Identify the blood parasite species.
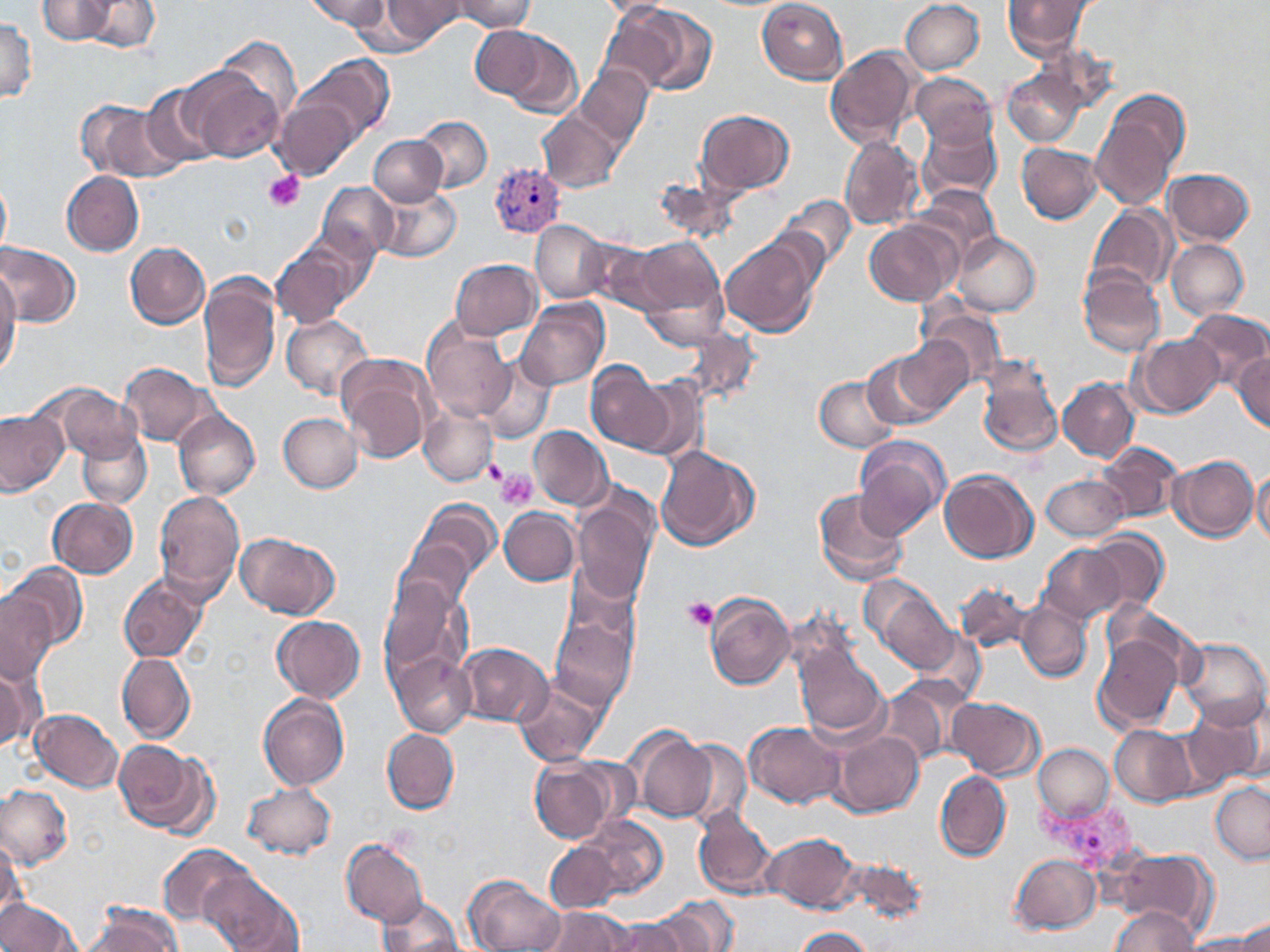

Plasmodium vivax.

field of view = single
Plasmodium vivax-infected red blood cell locations = approximate bounding boxes as [x1, y1, x2, y2] in pixels: [489, 162, 565, 238], [1030, 797, 1146, 877]
platelet locations = approximate bounding boxes as [x1, y1, x2, y2] in pixels: [263, 172, 305, 213], [483, 457, 508, 485], [497, 470, 538, 510], [682, 596, 719, 631]
magnification = 1000x
image size = 1270×952 pixels
uninfected red blood cell locations = approximate bounding boxes as [x1, y1, x2, y2] in pixels: [36, 0, 119, 44], [80, 0, 159, 54], [308, 0, 391, 29], [377, 0, 468, 47], [452, 0, 535, 32], [901, 0, 985, 75], [1000, 0, 1097, 61], [757, 1, 848, 83], [608, 3, 714, 100], [2, 14, 37, 103], [471, 26, 545, 98], [496, 31, 582, 119], [826, 47, 919, 149], [296, 56, 390, 145], [575, 65, 651, 149], [183, 66, 285, 164], [1003, 66, 1089, 149], [910, 73, 998, 151], [139, 84, 223, 171], [1091, 87, 1192, 214], [276, 97, 361, 180], [74, 99, 174, 181], [696, 109, 794, 195], [537, 112, 619, 192], [414, 117, 492, 193], [916, 118, 1004, 206], [369, 134, 447, 206], [838, 135, 924, 231], [1016, 142, 1101, 223], [1164, 167, 1255, 246], [61, 171, 144, 256], [0, 177, 11, 256], [317, 182, 398, 261], [913, 184, 1003, 267], [375, 186, 461, 264], [774, 192, 856, 280], [1086, 208, 1175, 295], [531, 219, 607, 302], [865, 220, 960, 306], [953, 231, 1040, 317], [720, 235, 820, 339], [630, 237, 726, 340], [1166, 239, 1250, 320], [125, 242, 210, 327], [0, 243, 82, 327], [272, 246, 355, 328], [452, 259, 541, 339], [1078, 268, 1164, 358], [0, 271, 21, 375], [199, 273, 280, 392], [517, 299, 609, 390], [920, 304, 1009, 389], [1183, 309, 1269, 391], [281, 313, 374, 400], [422, 319, 516, 423], [679, 322, 761, 406], [894, 333, 973, 415], [1130, 334, 1222, 418], [366, 336, 513, 449], [861, 347, 955, 433], [1232, 350, 1270, 433], [336, 352, 438, 463], [477, 356, 556, 443], [977, 357, 1065, 460], [120, 362, 210, 446], [587, 363, 675, 452], [815, 376, 901, 451], [1058, 378, 1138, 461], [40, 384, 141, 460], [421, 405, 497, 485], [173, 408, 260, 500], [0, 409, 69, 497], [279, 413, 364, 492], [529, 425, 611, 511], [77, 431, 150, 507], [852, 436, 948, 538], [1099, 442, 1182, 523], [655, 444, 761, 552], [1168, 454, 1259, 542], [939, 469, 1038, 563], [1249, 469, 1269, 548], [1041, 472, 1129, 542], [812, 487, 911, 587], [153, 489, 247, 602], [571, 491, 657, 609], [48, 497, 138, 578], [397, 497, 503, 616], [498, 507, 580, 585], [1086, 530, 1168, 613], [236, 533, 340, 621], [1038, 543, 1130, 626], [3, 562, 87, 654], [118, 573, 207, 663], [863, 576, 961, 675], [379, 577, 472, 697], [955, 583, 1038, 657], [705, 592, 796, 690], [0, 594, 55, 687], [1016, 600, 1092, 684], [549, 609, 639, 713], [272, 617, 366, 703], [1093, 633, 1183, 729], [1180, 637, 1269, 729], [458, 641, 552, 727], [795, 648, 891, 744], [389, 651, 477, 736], [116, 652, 195, 743], [0, 657, 42, 749], [877, 676, 972, 768], [514, 680, 607, 765], [257, 691, 350, 792], [948, 696, 1043, 780], [1182, 704, 1265, 790], [30, 709, 123, 791], [743, 721, 845, 809], [1110, 726, 1198, 809], [382, 729, 460, 812], [835, 729, 923, 816], [633, 730, 717, 824], [681, 739, 749, 827], [111, 740, 216, 838], [1032, 743, 1115, 823], [528, 756, 619, 843], [935, 770, 1011, 861], [1209, 779, 1270, 863], [243, 783, 337, 861], [0, 784, 71, 871], [694, 809, 780, 899], [576, 815, 669, 904], [765, 833, 858, 912], [0, 837, 27, 928], [341, 839, 431, 929], [545, 842, 623, 912], [158, 844, 254, 929], [1113, 848, 1215, 932], [1010, 853, 1102, 935], [201, 873, 302, 951], [464, 873, 565, 952], [373, 895, 466, 952], [1, 898, 80, 951], [655, 900, 741, 951], [80, 902, 183, 952], [1106, 906, 1199, 951], [536, 908, 638, 951], [568, 913, 674, 952], [606, 919, 687, 950], [790, 926, 877, 951], [1182, 931, 1270, 951]
stain = May-Grünwald-Giemsa
modality = light microscopy
preparation = thin blood film